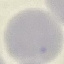
result = negative for malaria parasites
image type = automatically extracted cell patch, resized to 64 × 64 pixels
stain = Giemsa
preparation = thin blood smear
capture = smartphone through the microscope eyepiece